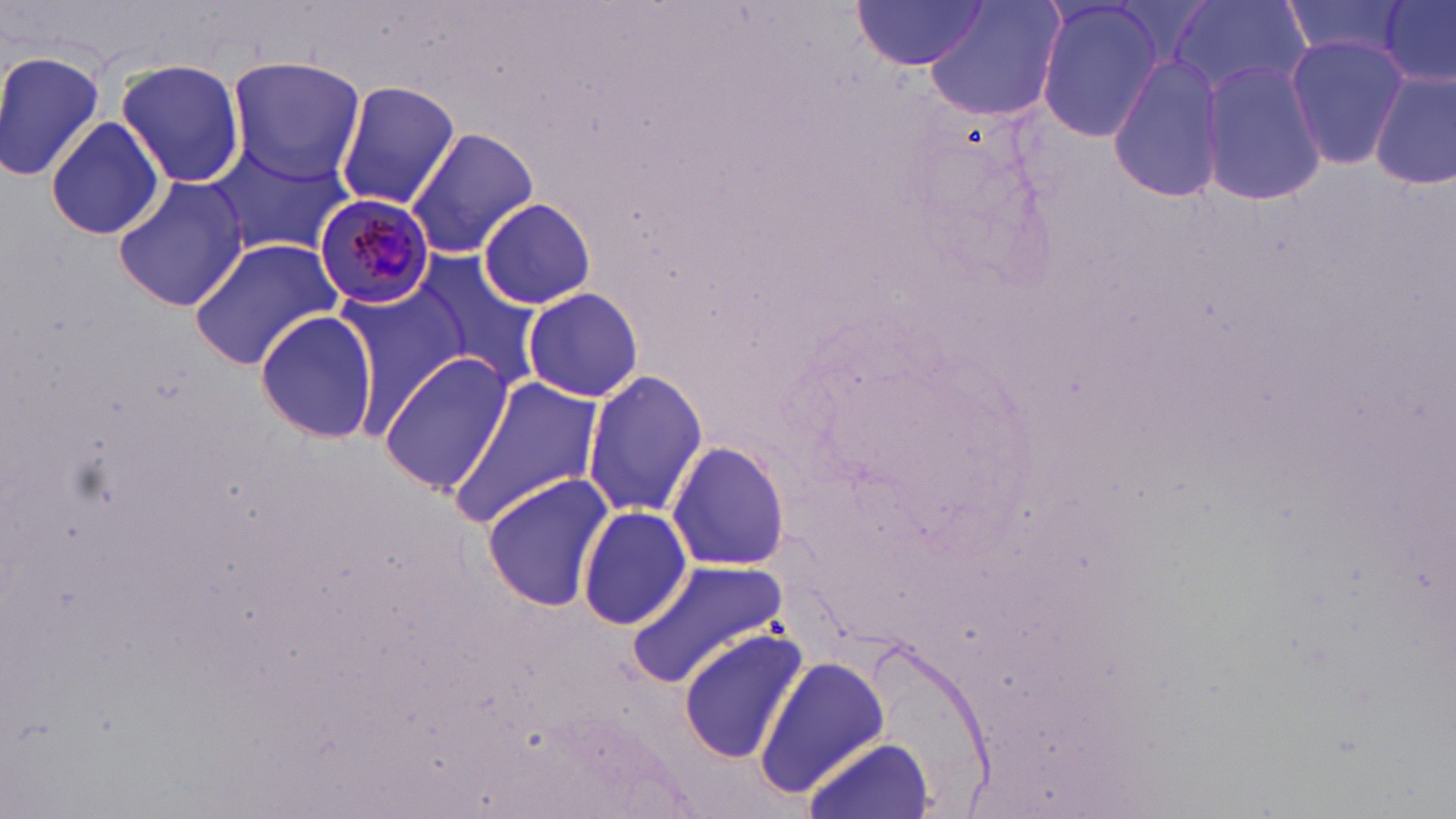
Approximate bounding boxes as (x1,y1)-(x2,y2) corner pairs in pixels. Plasmodium malariae-infected red blood cell locations: (315,193)-(436,310). Uninfected red blood cell locations: (922,0)-(1066,124), (1171,0)-(1309,106), (1378,0)-(1454,83), (852,1)-(988,72), (1276,1)-(1417,64), (1034,2)-(1171,144), (1284,34)-(1408,169), (0,48)-(107,180), (1106,53)-(1228,206), (225,56)-(367,181), (115,58)-(247,188), (1194,60)-(1329,206), (1371,68)-(1455,191), (334,81)-(460,212), (45,115)-(165,240), (408,122)-(536,258), (209,140)-(354,257), (112,173)-(250,312), (477,196)-(596,310), (187,237)-(344,369), (403,251)-(544,386), (335,286)-(461,432), (522,286)-(646,404), (252,310)-(379,443), (378,350)-(514,496), (583,370)-(708,517), (448,374)-(606,529), (667,440)-(792,572), (482,474)-(613,612), (577,505)-(694,630), (624,558)-(792,686), (678,628)-(806,762), (759,657)-(892,794), (804,734)-(936,819). Slide-level diagnosis: Plasmodium malariae. Captured at 1000x magnification. Thin blood smear. Light microscopy. Image is 1456×819 pixels. One field of a larger specimen. May-Grünwald-Giemsa stain.